Report the malaria status of this cell.
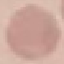

Uninfected.

Giemsa-stained preparation. Photographed with a smartphone camera at the microscope eyepiece. Thin smear of blood. Automatically extracted cell patch, resized to 64 × 64 pixels.